Point out each leukocyte.
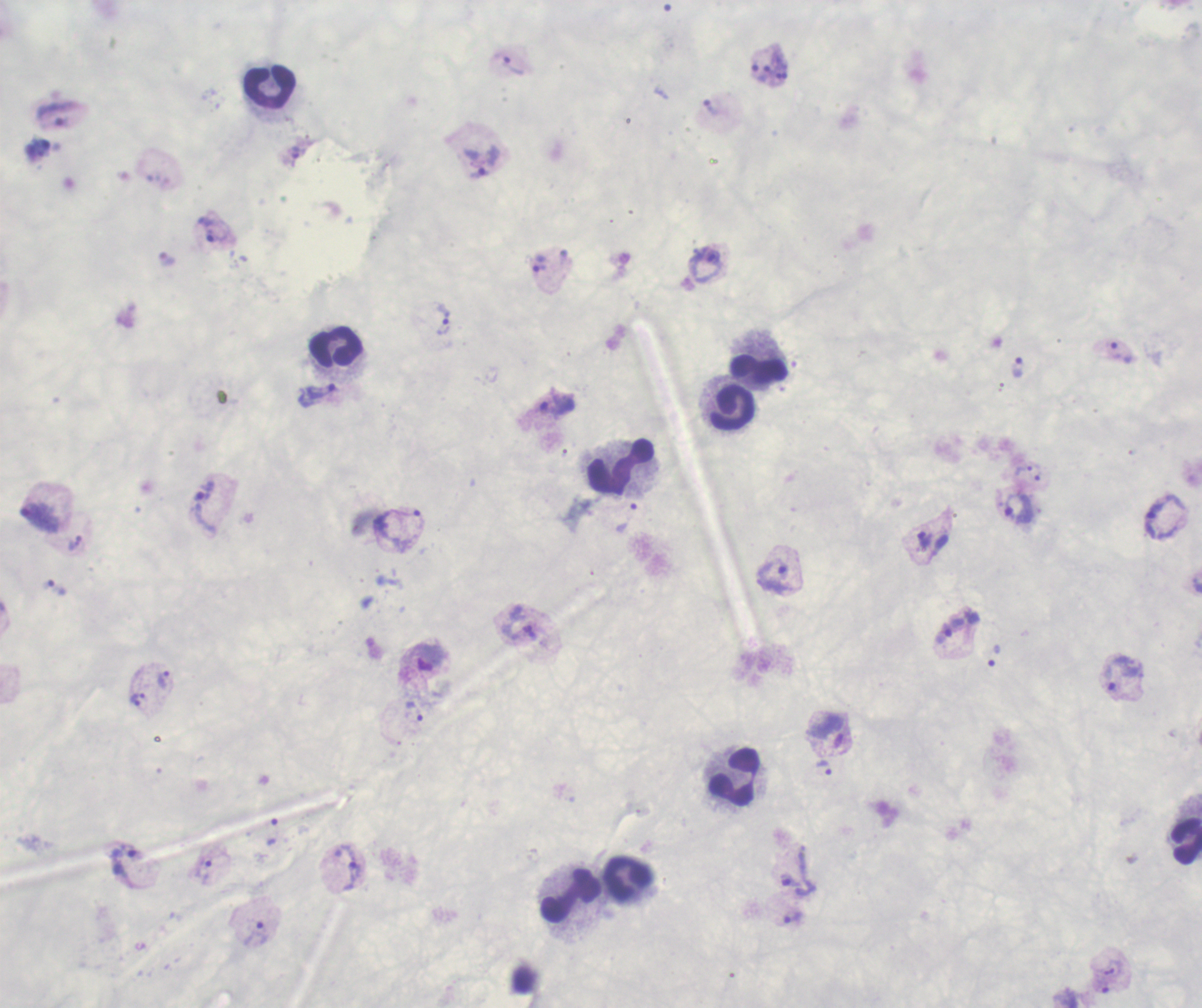

Approximate centers as (x, y) in pixels.
Leukocytes: (269, 84), (335, 345), (758, 369), (734, 406), (619, 466), (734, 776), (1187, 841), (627, 878), (570, 894).

result: malaria parasites detected
field_of_view: one from this slide
context: previously used in an actual diagnosis
magnification: 100x
background_quality: poor
stain: Romanowsky
image_size: 1202×1008 pixels
preparation: thick blood film
trophozoite_locations: 'approximate centers as (x, y) in pixels: (513, 65), (764, 73), (710, 107), (56, 114), (295, 152), (479, 173), (209, 221), (217, 237), (707, 258), (539, 267), (443, 321), (1115, 351), (1017, 367), (316, 394), (557, 404), (1023, 469), (1038, 473), (205, 506), (1018, 507), (408, 513), (39, 516), (1155, 518), (926, 539), (74, 541), (782, 570), (48, 584), (949, 631), (429, 657), (1108, 678), (163, 679), (137, 696), (136, 703), (414, 711), (825, 768), (134, 851), (205, 872), (353, 872), (790, 881), (794, 917), (255, 933)'